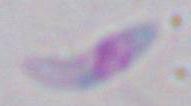

magnification = 1000x
modality = photomicrograph
identification = Toxoplasma gondii